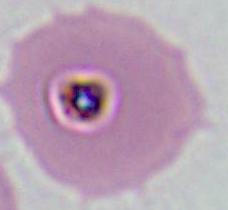

Summary:
  - Magnification: 400x or 1000x
  - Modality: micrograph
  - Identification: Plasmodium